Comment on the morphology of the erythrocytes.
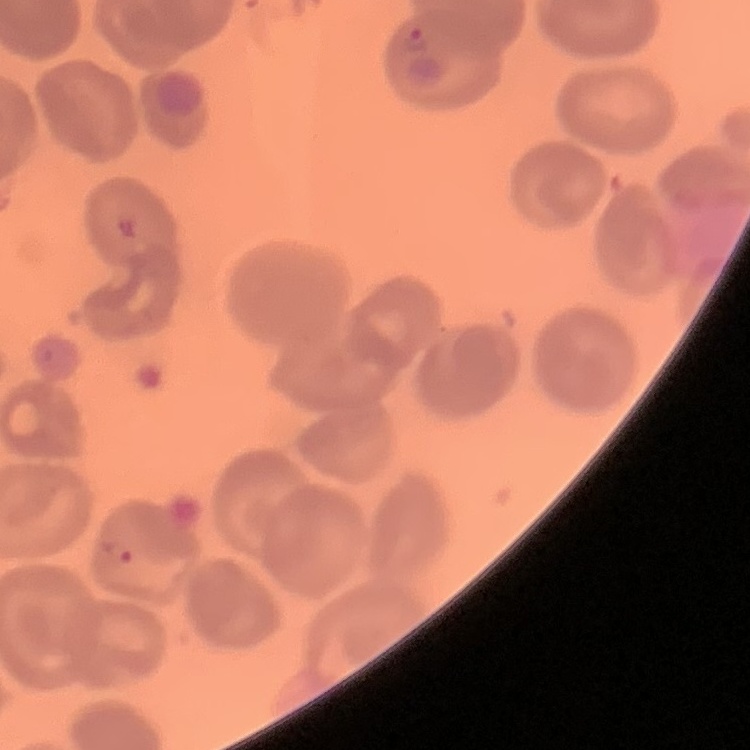

They show no rouleaux formation.

Thin blood smear. Stained with either Field's or Giemsa. One tile cut from a larger photomicrograph.